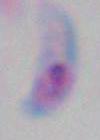
Summary:
  - Magnification: 1000x
  - Identification: Toxoplasma gondii
  - Modality: photomicrograph